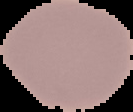
Summary:
  - Preparation: thin blood smear
  - Malaria status: uninfected
  - Image size: 133×112 pixels
  - Image type: segmented cell region with the area outside set to black